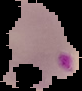
Cell region segmented out of the field of view; the surrounding area is masked to black. Result: malaria parasites detected. From a thin blood film. Image is 82×91 pixels.